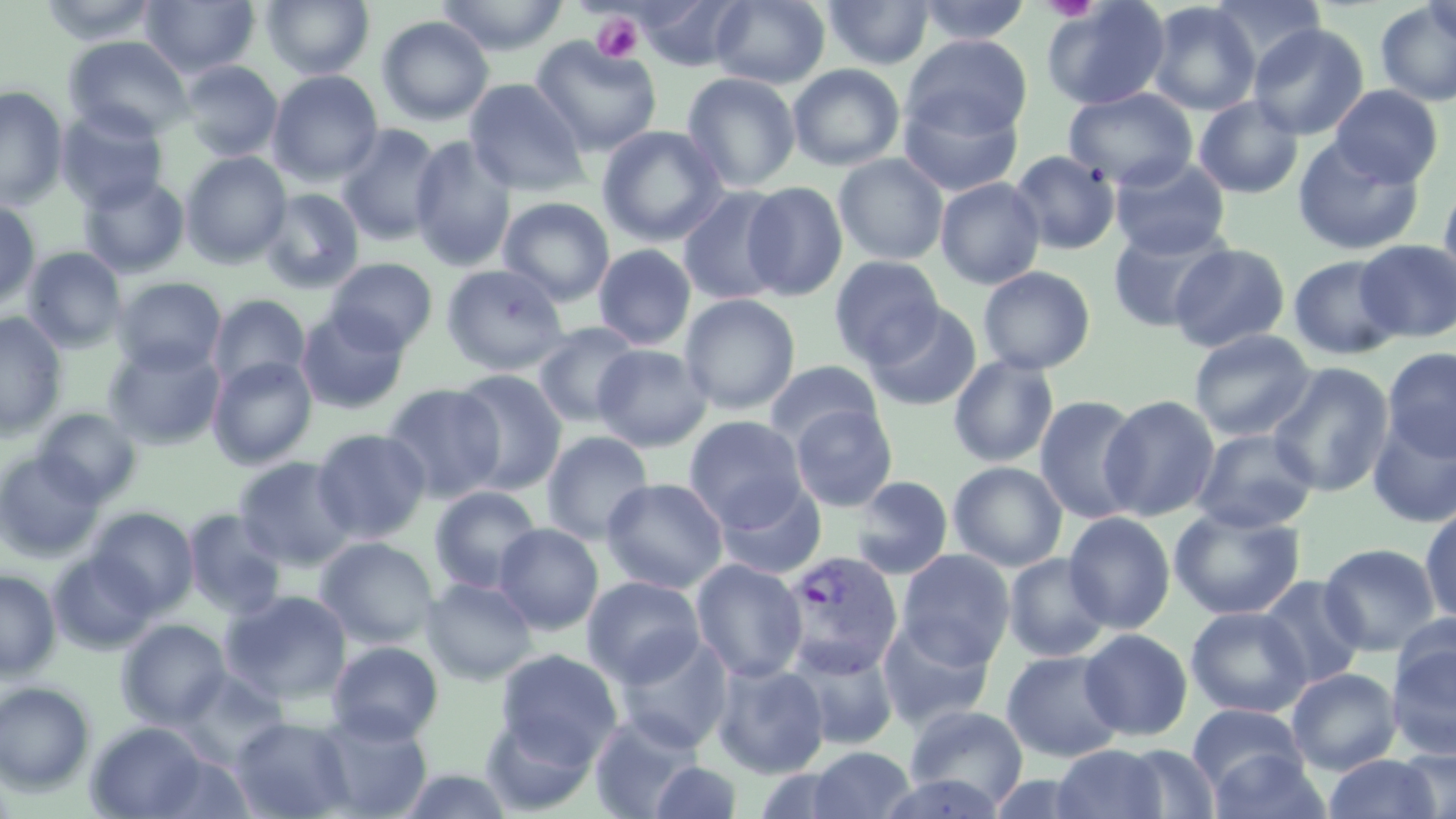
slide-level diagnosis = Plasmodium vivax
platelet locations = approximate bounding boxes as (x1,y1)-(x2,y2) corner pairs in pixels: (1043,0)-(1101,21), (592,12)-(644,62)
preparation = thin blood film
field of view = one of a larger specimen
Plasmodium vivax-infected red blood cell locations = approximate bounding boxes as (x1,y1)-(x2,y2) corner pairs in pixels: (778,551)-(904,678)
image size = 1456×819 pixels
magnification = 1000x
stain = May-Grünwald-Giemsa
uninfected red blood cell locations = approximate bounding boxes as (x1,y1)-(x2,y2) corner pairs in pixels: (37,0)-(163,45), (140,0)-(259,78), (261,0)-(374,80), (435,0)-(569,56), (636,0)-(748,70), (710,0)-(830,89), (822,0)-(934,70), (915,0)-(1032,45), (1042,0)-(1171,111), (1208,0)-(1327,73), (1422,0)-(1456,45), (1146,1)-(1261,116), (1375,2)-(1456,107), (698,5)-(824,166), (376,16)-(494,125), (1248,23)-(1369,140), (63,35)-(193,141), (902,35)-(1032,140), (530,36)-(662,156), (180,60)-(283,161), (787,63)-(905,172), (267,70)-(383,186), (681,72)-(801,192), (464,79)-(589,197), (1329,84)-(1444,187), (0,85)-(68,210), (1063,87)-(1198,191), (898,90)-(1024,198), (1194,95)-(1304,199), (56,106)-(169,213), (337,124)-(445,245), (597,125)-(728,247), (409,136)-(517,272), (1292,137)-(1425,255), (1010,150)-(1121,255), (181,152)-(292,267), (833,153)-(949,266), (1110,156)-(1231,259), (78,173)-(189,278), (935,177)-(1045,289), (1439,179)-(1456,293), (741,181)-(849,301), (677,187)-(789,306), (259,188)-(366,294), (498,197)-(615,306), (0,199)-(41,312), (1107,222)-(1232,333), (1355,239)-(1456,343), (1168,243)-(1291,353), (593,244)-(697,350), (22,246)-(127,353), (1288,254)-(1405,360), (829,256)-(945,367), (325,257)-(438,354), (441,264)-(569,376), (978,266)-(1095,375), (112,276)-(226,375), (208,293)-(311,391), (679,294)-(800,415), (865,302)-(983,411), (296,308)-(410,414), (0,313)-(67,438), (532,321)-(643,429), (1189,329)-(1316,442), (103,340)-(226,450), (592,344)-(712,452), (1382,347)-(1456,462), (948,355)-(1059,468), (207,356)-(317,469), (764,359)-(884,449), (1267,362)-(1394,497), (451,369)-(569,494), (381,383)-(505,503), (1100,394)-(1220,522), (1033,395)-(1145,524), (789,403)-(898,512), (33,408)-(143,505), (1367,411)-(1456,528), (685,416)-(808,528), (311,428)-(431,543), (1192,429)-(1319,533), (541,431)-(655,545), (1,451)-(105,561), (234,456)-(357,570), (948,461)-(1068,572), (849,475)-(953,580), (602,478)-(728,593), (714,478)-(827,580), (429,486)-(543,594), (1420,506)-(1456,626), (89,507)-(199,613), (1169,507)-(1306,621), (183,509)-(288,618), (1063,512)-(1176,634), (494,522)-(603,635), (315,537)-(439,649), (1319,542)-(1442,656), (896,549)-(1015,670), (49,552)-(158,654), (1003,553)-(1112,662), (691,559)-(807,682), (0,570)-(60,678), (582,575)-(706,688), (1258,575)-(1368,690), (421,578)-(538,685), (220,590)-(353,706), (1186,606)-(1311,718), (1391,611)-(1456,703), (117,619)-(230,728), (877,619)-(995,732), (1078,628)-(1193,741), (613,633)-(733,752), (1386,635)-(1456,759), (785,639)-(900,751), (327,641)-(444,744), (495,649)-(622,766), (1001,650)-(1126,762), (711,661)-(829,779), (1287,668)-(1402,775), (176,670)-(289,766), (0,681)-(96,795), (1187,703)-(1308,796), (904,704)-(1028,811), (312,711)-(432,818), (589,711)-(703,819), (481,713)-(596,813), (231,716)-(354,819), (86,721)-(210,818), (1052,744)-(1169,819), (1116,744)-(1220,818), (806,746)-(916,819), (1395,747)-(1456,818), (1206,749)-(1332,819), (1323,754)-(1440,818), (650,761)-(742,818), (395,768)-(515,818), (877,773)-(1006,819)
modality = light microscopy